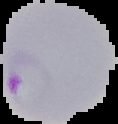
Malaria status: parasitized. From a thin blood smear. Image is 118×124 pixels. The area outside the segmented cell region is set to black.